Assess this cell for malaria.
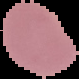
Uninfected.

The area outside the segmented cell region is set to black. From a thin blood smear. Image is 79×79 pixels.